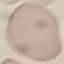

result = no malaria parasites detected
preparation = thin blood film
image type = cell patch, automatically extracted from a larger field of view and resized to 64 × 64 pixels
capture = smartphone camera at the microscope eyepiece
stain = Giemsa